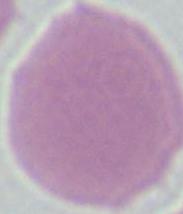
A red blood cell is seen. Captured at 1000x magnification. Photomicrograph.